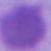

{
  "identification": "red blood cell",
  "magnification": "1000x",
  "modality": "micrograph"
}